Classify this cell by malaria status.
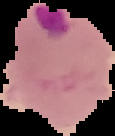

It is parasitized.

Summary:
  - Preparation: thin blood film
  - Image type: segmented cell region on a black background
  - Image size: 115×136 pixels